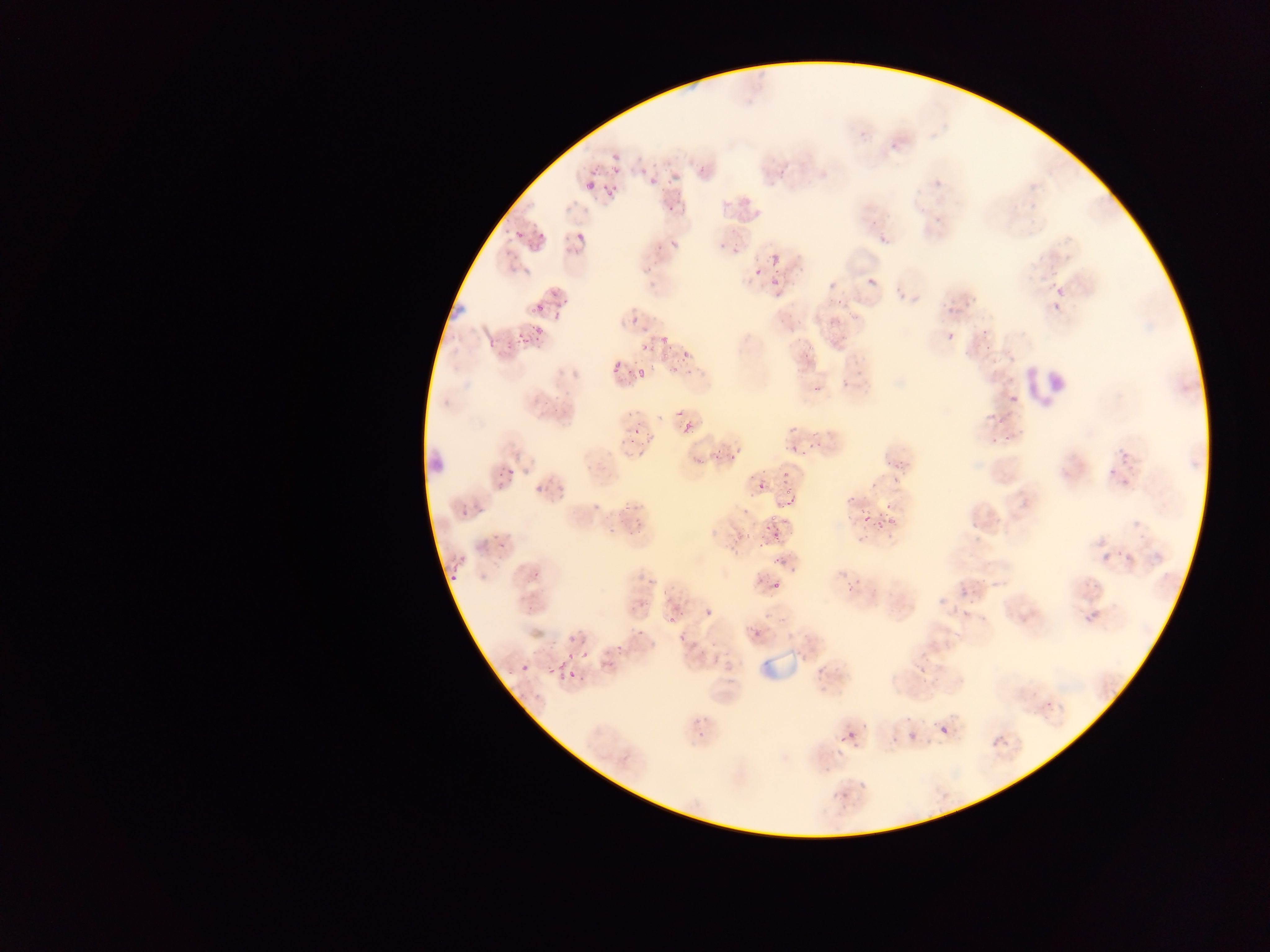
Approximate bounding boxes as [left, top, right, bottom] in pixels. Leukocyte locations: [1013, 365, 1061, 404], [430, 447, 451, 476]. Malaria parasite locations: [610, 146, 624, 163], [607, 161, 624, 176], [588, 164, 599, 178], [650, 177, 658, 185], [586, 181, 595, 191], [603, 181, 620, 199], [513, 230, 523, 239], [577, 232, 586, 241], [669, 236, 677, 252], [874, 236, 888, 247], [648, 243, 661, 254], [569, 245, 580, 256], [771, 254, 779, 262], [755, 267, 762, 276], [765, 272, 780, 291], [867, 278, 876, 287], [1051, 281, 1064, 297], [551, 287, 561, 296], [913, 295, 920, 303], [1051, 299, 1061, 316], [532, 303, 544, 315], [826, 313, 838, 332], [628, 317, 637, 326], [978, 321, 991, 339], [528, 325, 545, 346], [511, 329, 530, 350], [947, 332, 956, 341], [657, 336, 674, 346], [485, 337, 502, 350], [503, 340, 519, 353], [633, 342, 650, 356], [798, 347, 810, 358], [681, 350, 690, 359], [657, 352, 676, 363], [631, 362, 649, 386], [611, 363, 619, 372], [814, 385, 823, 394], [670, 407, 683, 420], [989, 414, 1002, 427], [627, 417, 648, 439], [680, 425, 692, 445], [990, 434, 1000, 446], [1002, 435, 1015, 442], [621, 441, 631, 455], [806, 443, 817, 455], [1117, 447, 1131, 466], [789, 448, 799, 458], [711, 450, 721, 462], [888, 451, 909, 479], [729, 453, 738, 463], [502, 464, 523, 476], [1106, 464, 1118, 477], [782, 470, 793, 484], [1118, 470, 1133, 487], [532, 472, 553, 499], [753, 472, 770, 492], [782, 488, 797, 506], [585, 491, 611, 514], [848, 496, 856, 503], [454, 498, 473, 516], [473, 500, 484, 513], [882, 500, 893, 512], [859, 510, 868, 524], [631, 511, 652, 529], [880, 512, 892, 526], [606, 516, 626, 537], [760, 517, 774, 528], [729, 524, 748, 541], [493, 526, 511, 549], [770, 530, 778, 543], [754, 535, 770, 555], [727, 541, 742, 556], [1101, 551, 1112, 564], [771, 556, 789, 572], [531, 564, 544, 588], [447, 571, 458, 584], [845, 574, 858, 593], [770, 578, 779, 588], [954, 579, 969, 597], [949, 598, 962, 611], [700, 602, 710, 618], [662, 607, 681, 627], [1083, 609, 1098, 626], [752, 629, 761, 638], [679, 632, 686, 641], [613, 634, 628, 660], [562, 640, 573, 671], [580, 650, 588, 659], [546, 663, 555, 675], [521, 664, 530, 673], [556, 671, 565, 681], [570, 671, 581, 682], [845, 716, 870, 739], [938, 720, 951, 739], [908, 733, 917, 741], [987, 734, 1012, 755], [891, 736, 900, 745], [835, 745, 846, 758], [859, 781, 868, 790], [835, 791, 846, 801] | approximate [x, y] pixel centers of objects too small to bound: [938, 183]. Sample from Ghana. Thin blood film. One field of view. Mobile-phone photograph taken through the microscope. Image is 1270×952 pixels.